Outline each Plasmodium falciparum-infected red blood cell.
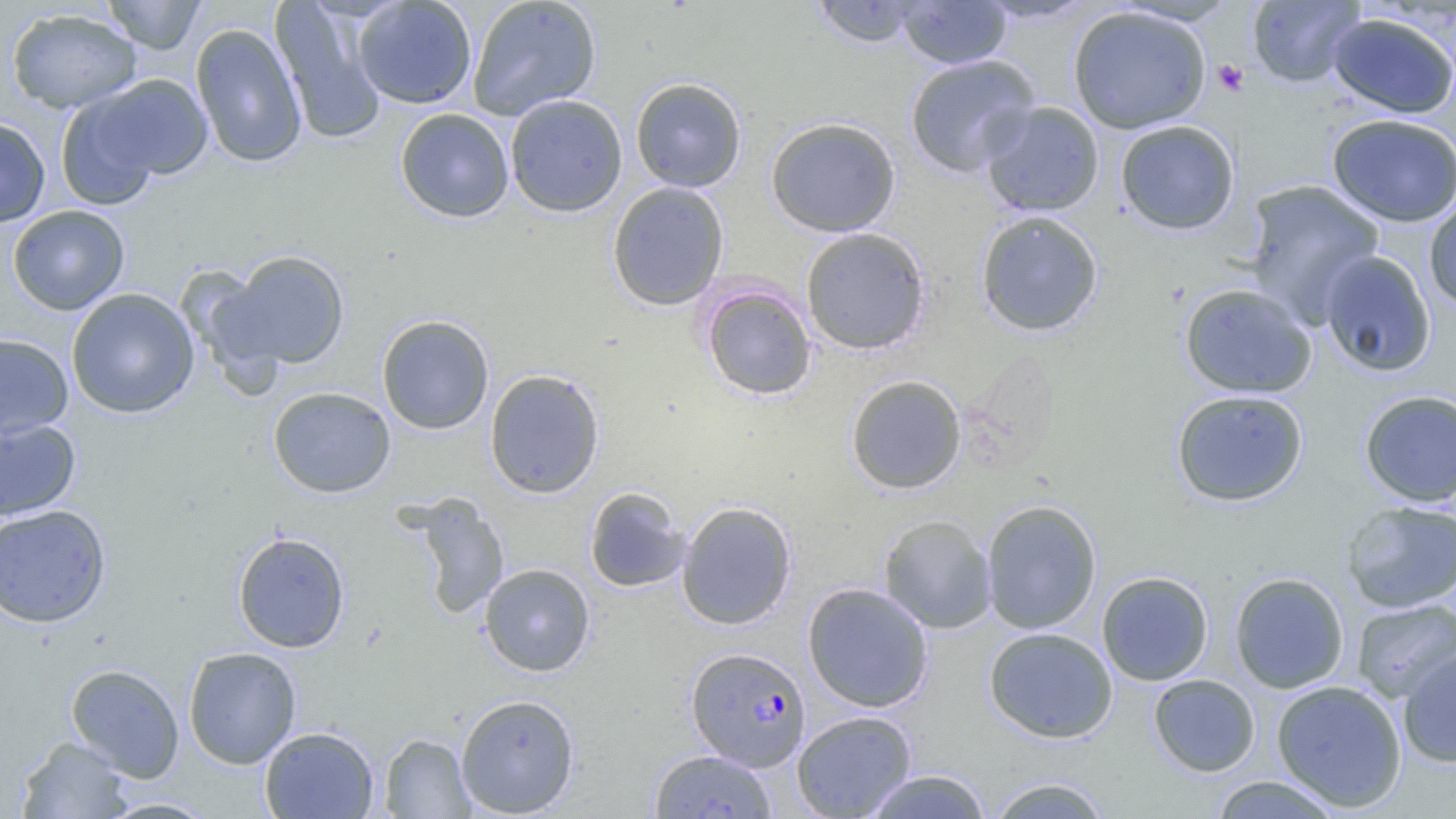

Approximate bounding boxes as [x1, y1, x2, y2] in pixels.
Plasmodium falciparum-infected red blood cells: [686, 647, 811, 771].

Platelet locations: [1213, 60, 1249, 97]. Uninfected red blood cell locations: [102, 0, 206, 55], [352, 0, 478, 109], [467, 0, 602, 121], [810, 0, 927, 48], [978, 0, 1098, 24], [1247, 0, 1366, 87], [271, 1, 387, 145], [896, 1, 1012, 69], [1068, 6, 1212, 134], [6, 8, 141, 113], [1326, 13, 1456, 119], [190, 23, 307, 169], [904, 54, 1041, 177], [92, 74, 212, 181], [630, 77, 747, 193], [55, 90, 164, 210], [504, 94, 628, 218], [980, 101, 1105, 217], [395, 108, 515, 223], [1327, 113, 1456, 227], [0, 116, 51, 227], [766, 117, 901, 237], [1115, 120, 1241, 236], [1242, 179, 1385, 327], [606, 181, 730, 311], [1423, 193, 1456, 312], [8, 205, 130, 315], [975, 209, 1104, 337], [800, 227, 931, 355], [1318, 250, 1437, 378], [217, 251, 350, 371], [699, 282, 817, 400], [1178, 283, 1317, 399], [66, 287, 200, 419], [376, 314, 495, 434], [0, 333, 74, 439], [484, 369, 605, 498], [845, 374, 966, 495], [268, 386, 396, 498], [1170, 388, 1309, 507], [1359, 390, 1456, 506], [0, 417, 81, 521], [584, 487, 691, 593], [407, 494, 510, 620], [980, 499, 1102, 635], [1341, 500, 1456, 613], [676, 501, 797, 631], [0, 504, 112, 628], [879, 514, 996, 634], [232, 531, 350, 653], [479, 563, 595, 677], [1096, 570, 1214, 686], [1229, 572, 1349, 694], [802, 582, 934, 713], [1351, 599, 1455, 703], [984, 627, 1118, 743], [1397, 645, 1456, 768], [183, 647, 302, 769], [65, 663, 185, 782], [1148, 673, 1261, 777], [1271, 679, 1408, 812], [455, 693, 581, 817], [791, 710, 918, 819], [259, 726, 378, 818], [379, 733, 475, 818], [16, 736, 133, 818], [649, 750, 778, 818], [863, 769, 993, 819], [1209, 775, 1343, 818], [984, 776, 1113, 819], [98, 797, 218, 818]. Slide-level diagnosis: Plasmodium falciparum. Light microscopy. One field of a larger specimen. Captured at 1000x magnification. Image is 1456×819 pixels. Thin blood film.